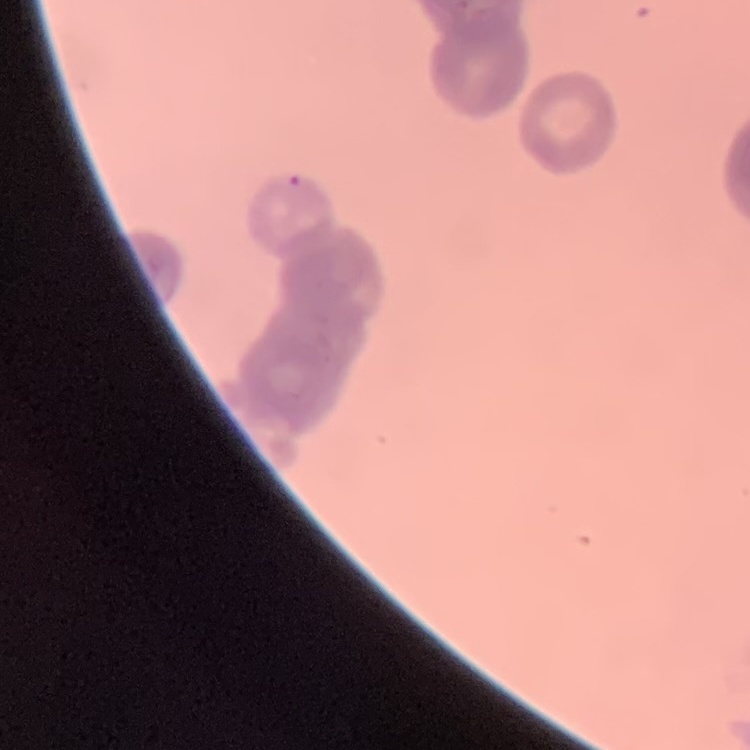

The red blood cells show rouleaux formation. Thin blood smear. Stained with either Field's or Giemsa. Square crop of a larger photomicrograph.